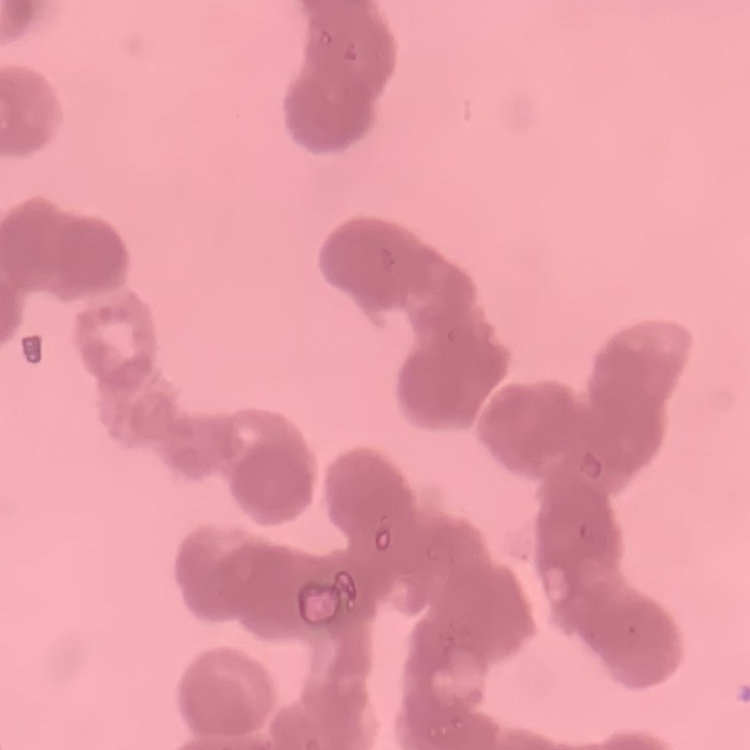

Summary:
  - Erythrocyte morphology: rouleaux formation
  - Preparation: thin peripheral smear
  - Image type: one tile cut from a larger photomicrograph
  - Stain: Field's or Giemsa